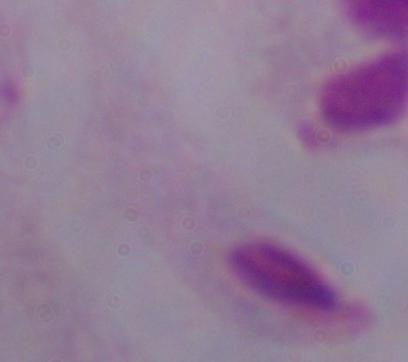

modality: photomicrograph
identification: trichomonad
magnification: 1000x